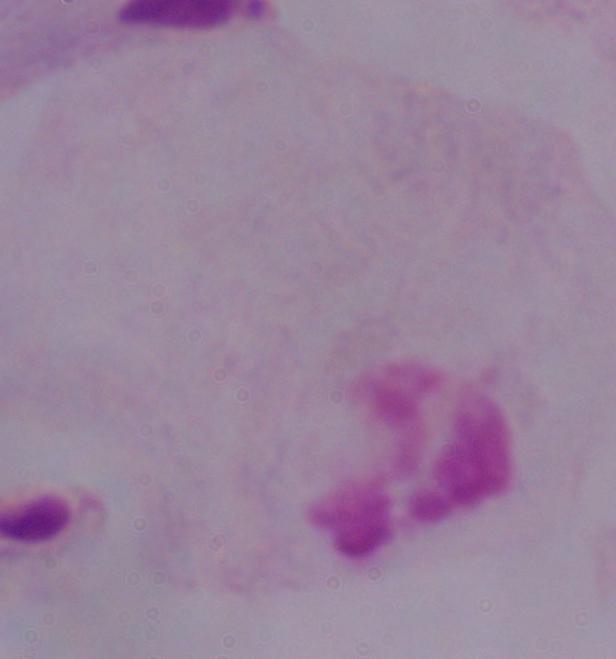

A trichomonad is shown. Photomicrograph. 1000x magnification.